Assess this cell for malaria.
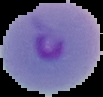

It is parasitized.

{
  "preparation": "thin blood film",
  "image_size": "103×97 pixels",
  "image_type": "segmented cell region on a black background"
}